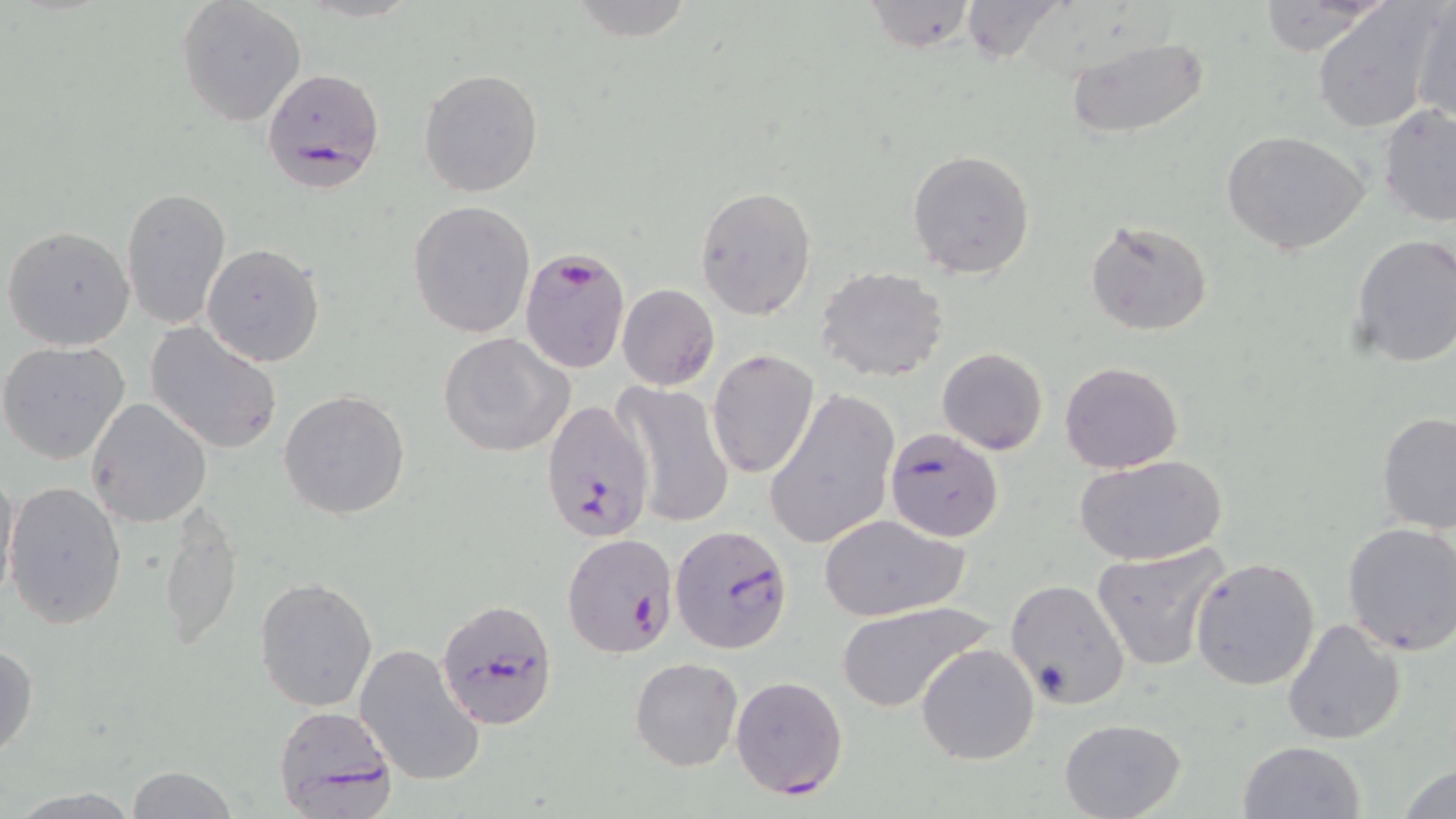 Approximate bounding boxes as (x1, y1, x2, y2) in pixels. Uninfected red blood cell locations: (1255, 0, 1387, 55), (566, 1, 698, 43), (861, 1, 977, 53), (177, 2, 304, 127), (1412, 2, 1455, 127), (955, 3, 1065, 63), (1312, 5, 1440, 133), (1066, 34, 1210, 141), (418, 69, 543, 196), (1378, 104, 1456, 227), (1221, 130, 1370, 255), (906, 150, 1036, 278), (694, 185, 816, 320), (121, 186, 230, 329), (408, 201, 533, 338), (1085, 217, 1214, 337), (3, 225, 134, 351), (1349, 233, 1456, 369), (202, 243, 325, 366), (816, 266, 950, 382), (616, 284, 719, 390), (145, 323, 283, 456), (437, 332, 575, 458), (0, 340, 132, 464), (937, 347, 1049, 455), (707, 349, 819, 478), (1059, 360, 1184, 474), (612, 381, 734, 529), (765, 387, 900, 551), (279, 388, 411, 521), (86, 397, 213, 528), (1374, 412, 1456, 535), (1077, 456, 1224, 567), (0, 466, 19, 608), (5, 482, 127, 630), (159, 503, 242, 652), (819, 515, 969, 621), (1341, 523, 1456, 656), (1092, 542, 1230, 672), (1190, 555, 1321, 690), (254, 576, 379, 711), (1006, 580, 1129, 709), (836, 601, 995, 714), (1282, 618, 1405, 743), (0, 641, 38, 763), (354, 643, 485, 787), (916, 643, 1041, 766), (630, 656, 742, 771), (1057, 718, 1186, 818), (1238, 739, 1367, 819), (1399, 764, 1455, 819), (126, 765, 238, 819), (3, 786, 146, 818). Plasmodium falciparum-infected red blood cell locations: (261, 68, 387, 191), (520, 247, 631, 378), (538, 399, 653, 544), (885, 428, 1003, 542), (670, 524, 794, 654), (562, 534, 679, 659), (438, 598, 560, 732), (730, 676, 851, 798), (272, 704, 400, 819). Slide-level diagnosis: Plasmodium falciparum. Light microscopy. Captured at 1000x magnification. One field of a larger specimen. Image is 1456×819 pixels. May-Grünwald-Giemsa stain. Thin blood smear.